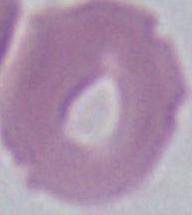

Summary:
  - Modality: photomicrograph
  - Magnification: 1000x
  - Identification: erythrocyte